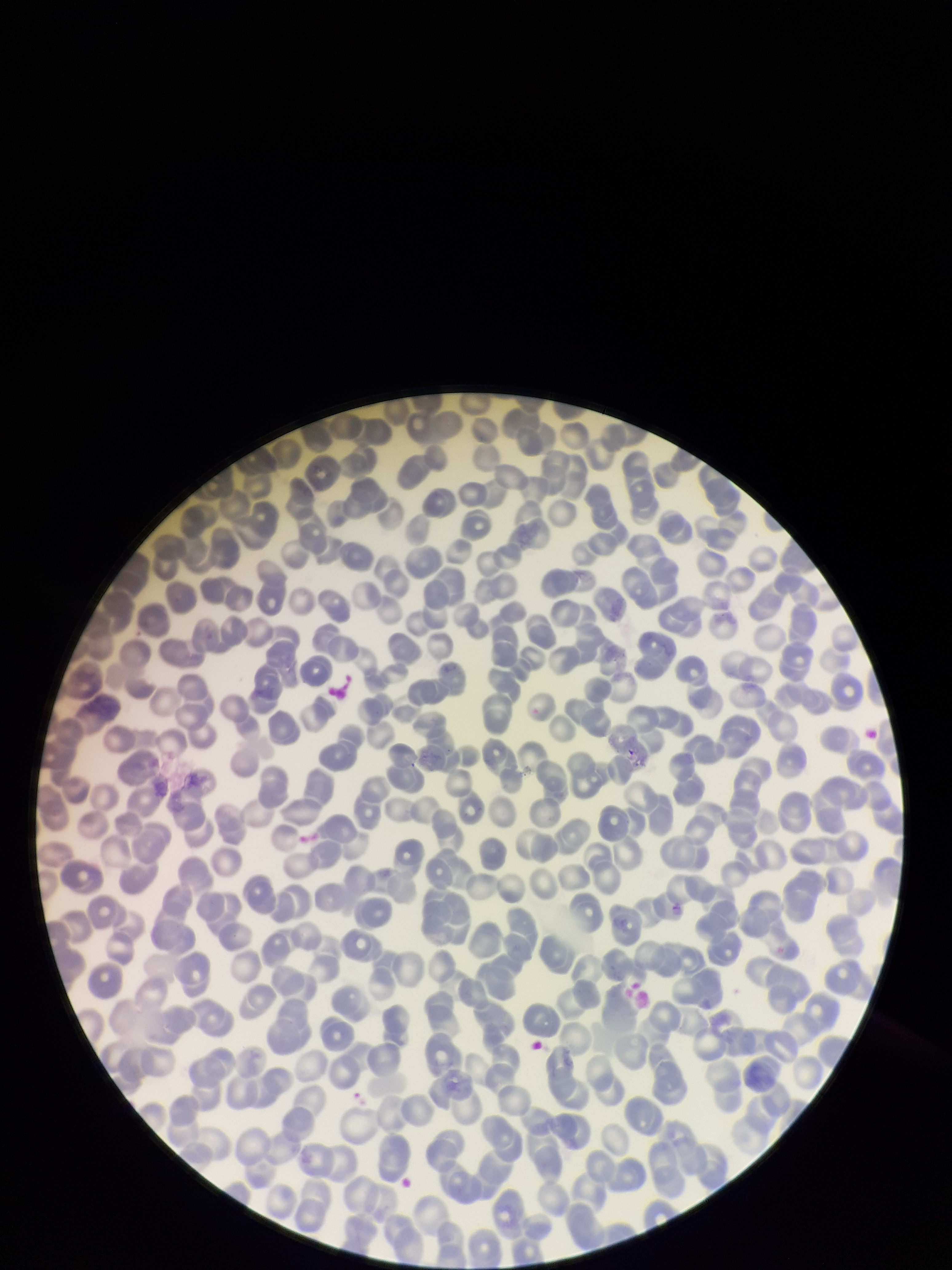

Photographed through the microscope eyepiece with a smartphone camera. Preparation: thin blood smear. Parasitized red blood cell count: 0. Parasitized red blood cells: none detected. Stained with Giemsa. Red blood cell count: 289. One field from this slide. Image is 952×1270 pixels. Patient malaria status: negative.